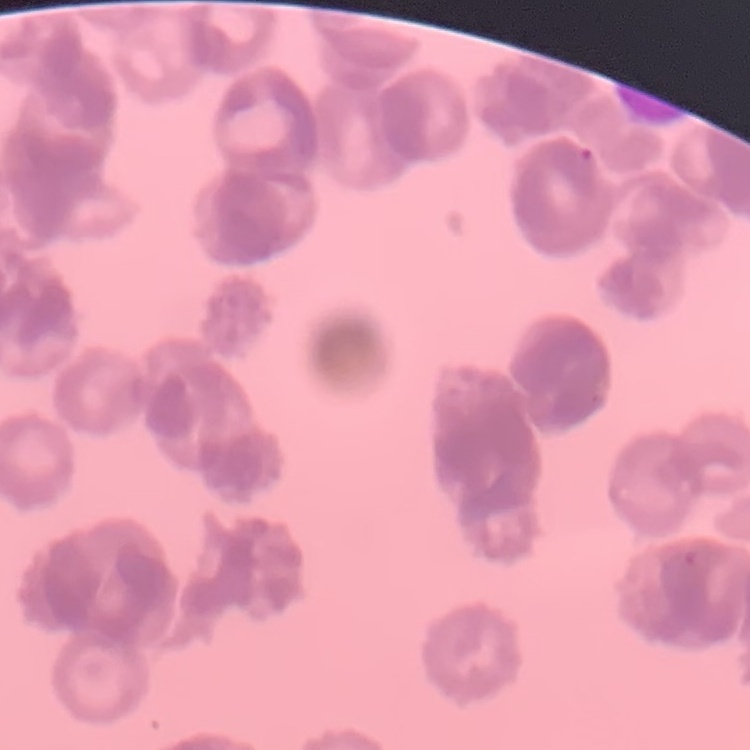

erythrocyte morphology = rouleaux formation
image type = one tile cut from a larger photomicrograph
stain = Field's or Giemsa
preparation = thin peripheral smear